Identify the blood parasite species.
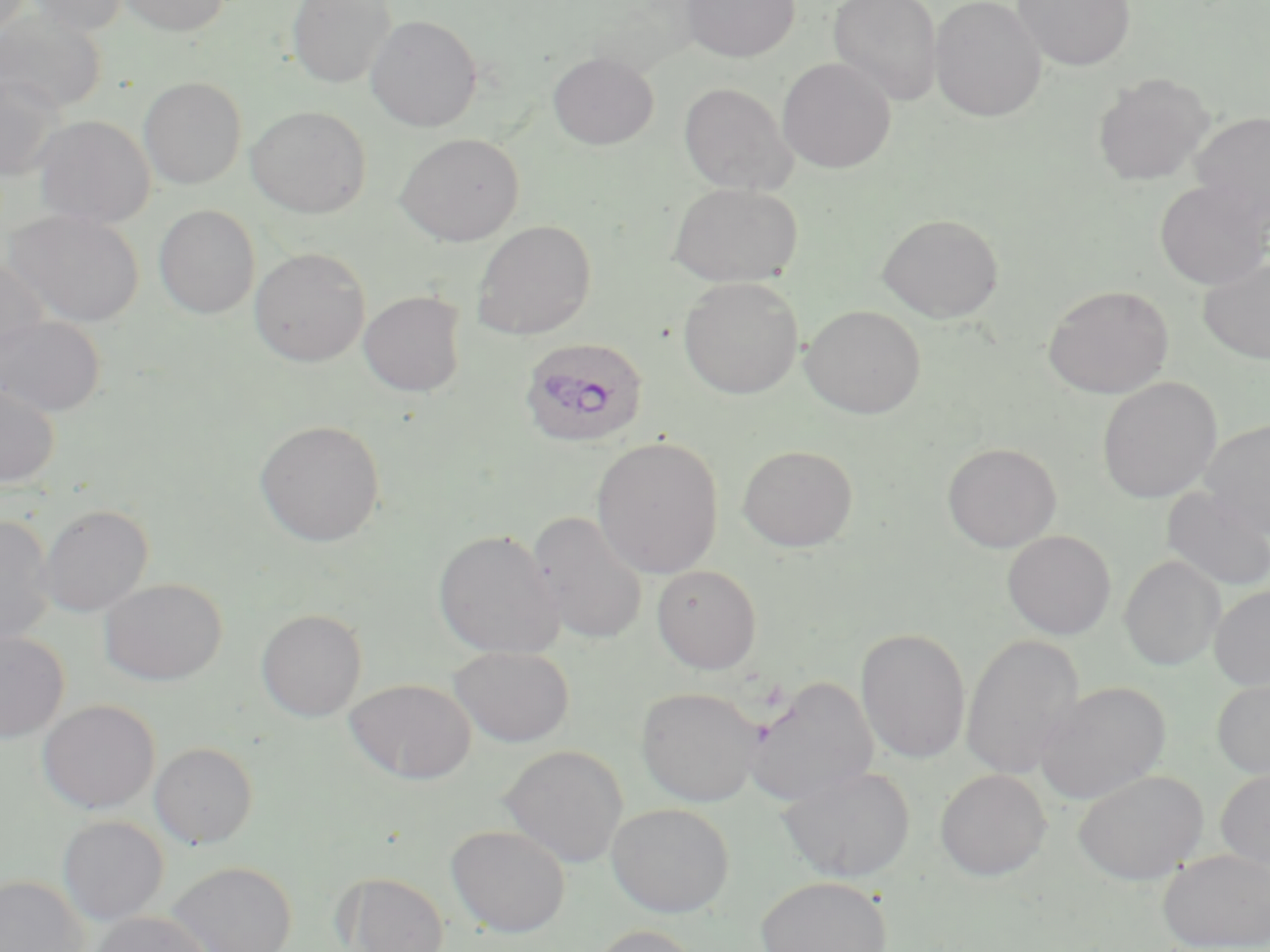
Plasmodium ovale.

Approximate bounding boxes as named x1/y1/x2/y2 corners in pixels. Uninfected red blood cell locations: (x1=1, y1=0, x2=34, y2=39), (x1=26, y1=0, x2=129, y2=35), (x1=117, y1=0, x2=230, y2=36), (x1=287, y1=0, x2=396, y2=88), (x1=681, y1=0, x2=800, y2=62), (x1=828, y1=0, x2=943, y2=106), (x1=929, y1=0, x2=1047, y2=122), (x1=1013, y1=0, x2=1135, y2=70), (x1=0, y1=11, x2=106, y2=115), (x1=365, y1=14, x2=483, y2=132), (x1=548, y1=52, x2=659, y2=149), (x1=777, y1=57, x2=895, y2=174), (x1=0, y1=72, x2=66, y2=180), (x1=1092, y1=72, x2=1214, y2=186), (x1=138, y1=76, x2=247, y2=189), (x1=678, y1=82, x2=796, y2=195), (x1=246, y1=105, x2=371, y2=218), (x1=1189, y1=110, x2=1270, y2=228), (x1=34, y1=116, x2=155, y2=229), (x1=395, y1=133, x2=525, y2=246), (x1=1154, y1=180, x2=1270, y2=291), (x1=668, y1=182, x2=803, y2=288), (x1=153, y1=204, x2=260, y2=319), (x1=5, y1=208, x2=145, y2=328), (x1=877, y1=213, x2=1004, y2=322), (x1=471, y1=220, x2=596, y2=340), (x1=249, y1=246, x2=370, y2=366), (x1=0, y1=255, x2=51, y2=368), (x1=1198, y1=255, x2=1270, y2=365), (x1=678, y1=276, x2=804, y2=400), (x1=1043, y1=284, x2=1173, y2=399), (x1=358, y1=290, x2=467, y2=397), (x1=800, y1=305, x2=927, y2=419), (x1=0, y1=314, x2=105, y2=417), (x1=1098, y1=376, x2=1222, y2=503), (x1=0, y1=380, x2=60, y2=487), (x1=1200, y1=418, x2=1270, y2=538), (x1=255, y1=420, x2=385, y2=547), (x1=591, y1=437, x2=724, y2=578), (x1=942, y1=442, x2=1061, y2=552), (x1=737, y1=444, x2=859, y2=552), (x1=1160, y1=487, x2=1270, y2=593), (x1=38, y1=504, x2=153, y2=616), (x1=528, y1=509, x2=649, y2=647), (x1=0, y1=516, x2=55, y2=646), (x1=432, y1=530, x2=564, y2=659), (x1=1003, y1=530, x2=1116, y2=640), (x1=1119, y1=554, x2=1224, y2=671), (x1=651, y1=564, x2=763, y2=673), (x1=99, y1=578, x2=227, y2=685), (x1=1209, y1=585, x2=1270, y2=690), (x1=256, y1=609, x2=367, y2=722), (x1=856, y1=627, x2=971, y2=764), (x1=0, y1=631, x2=69, y2=743), (x1=961, y1=633, x2=1084, y2=781), (x1=449, y1=645, x2=574, y2=747), (x1=744, y1=676, x2=877, y2=807), (x1=1212, y1=676, x2=1270, y2=779), (x1=344, y1=678, x2=476, y2=785), (x1=1035, y1=681, x2=1171, y2=804), (x1=636, y1=687, x2=762, y2=807), (x1=38, y1=699, x2=160, y2=813), (x1=149, y1=741, x2=259, y2=848), (x1=500, y1=744, x2=629, y2=867), (x1=778, y1=764, x2=916, y2=883), (x1=935, y1=768, x2=1050, y2=881), (x1=1215, y1=768, x2=1270, y2=874), (x1=1072, y1=769, x2=1209, y2=884), (x1=605, y1=802, x2=735, y2=917), (x1=57, y1=815, x2=168, y2=925), (x1=446, y1=823, x2=571, y2=937), (x1=1157, y1=849, x2=1270, y2=951), (x1=167, y1=860, x2=297, y2=952), (x1=340, y1=872, x2=449, y2=952), (x1=0, y1=875, x2=88, y2=952), (x1=756, y1=875, x2=893, y2=952), (x1=90, y1=911, x2=213, y2=952), (x1=585, y1=924, x2=707, y2=952). Plasmodium ovale-infected red blood cell locations: (x1=519, y1=337, x2=649, y2=448). 1000x magnification. Single field of view. Optical microscopy. Image is 1270×952 pixels. May-Grünwald-Giemsa stain. Thin blood smear.